Report the malaria status of this cell.
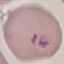
It is parasitized.

Cell patch, automatically extracted from a larger field of view and resized to 64 × 64 pixels. Acquired by smartphone through the microscope eyepiece. Giemsa stain. Thin blood smear.